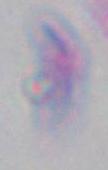
Captured at 1000x magnification. Micrograph. Toxoplasma gondii is shown.